State which parasite is depicted.
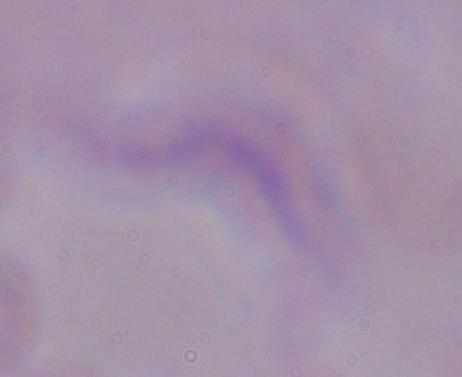
This is a trypanosome.

modality = micrograph
magnification = 1000x